Report the malaria status.
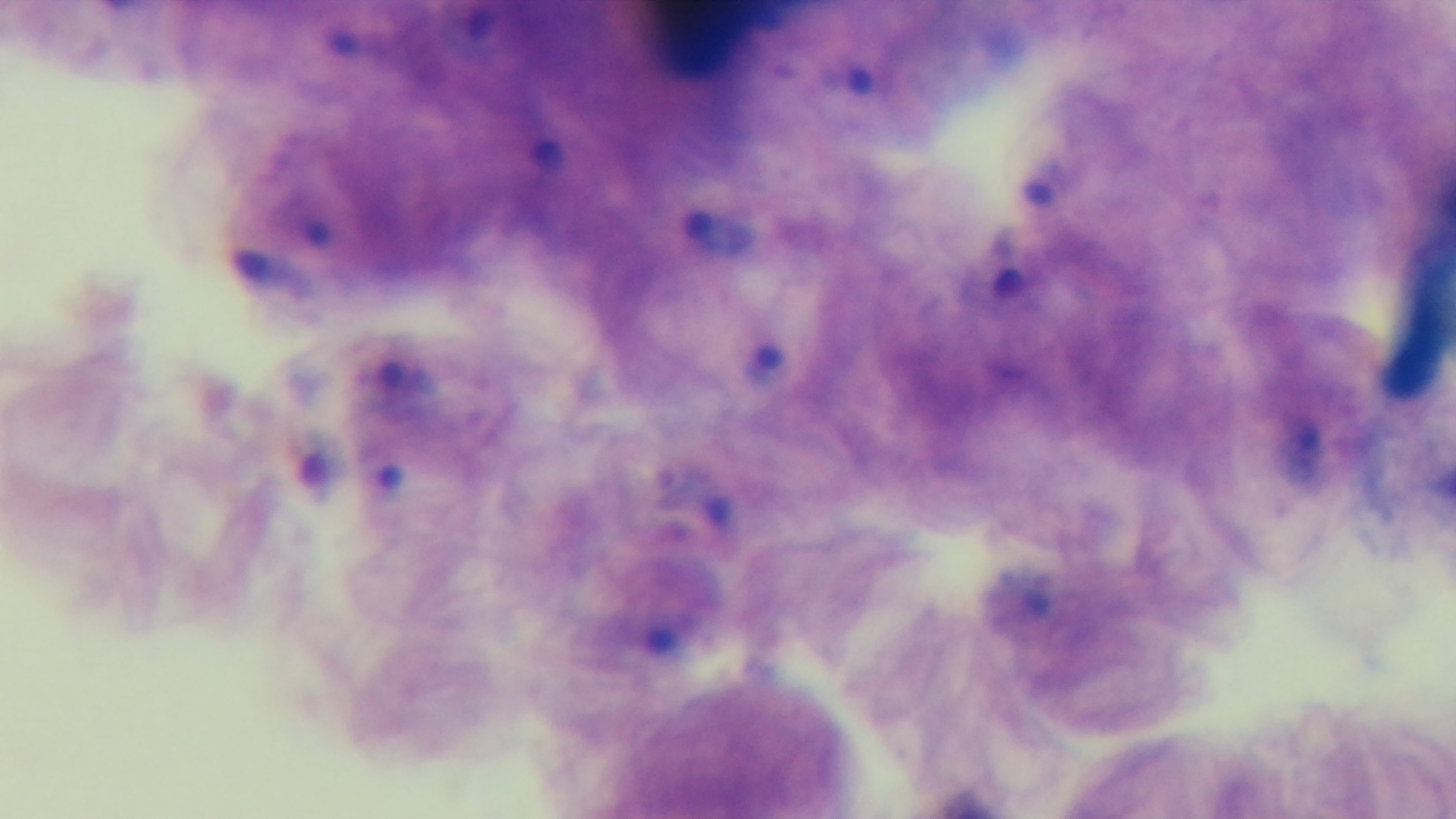

It is infected.

modality: light microscopy
capture: mounted 4K digital camera
preparation: thick smear
field_of_view: one from the slide
objective: 100x oil immersion
stain: Giemsa